Locate every leukocyte (white blood cell).
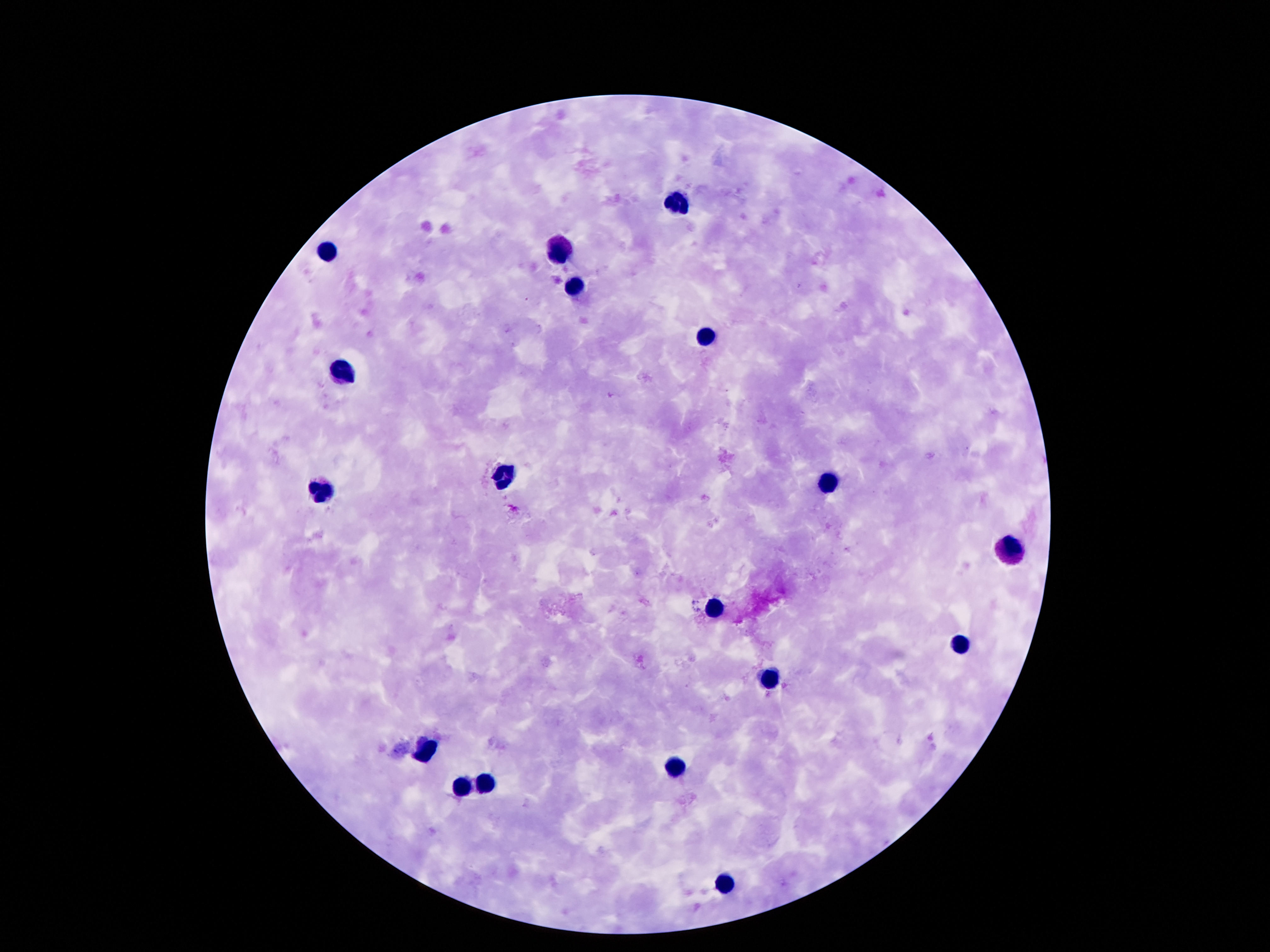
Approximate centers as [x, y] in pixels.
Leukocytes: [678, 200], [563, 251], [325, 252], [575, 285], [709, 336], [343, 369], [499, 473], [825, 481], [321, 492], [1012, 550], [716, 608], [961, 644], [771, 680], [426, 750], [676, 765], [488, 782], [460, 789], [727, 886].

Summary:
  - Stain: Giemsa
  - Magnification: 100x
  - Patient malaria status: negative
  - Image size: 1270×952 pixels
  - Preparation: thick blood smear
  - Field of view: one from this slide
  - Capture: smartphone camera through the microscope eyepiece